Assess this cell for malaria.
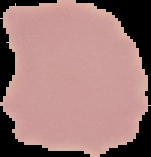

It is uninfected.

The area outside the segmented cell region is set to black. From a thin blood smear. Image is 151×157 pixels.